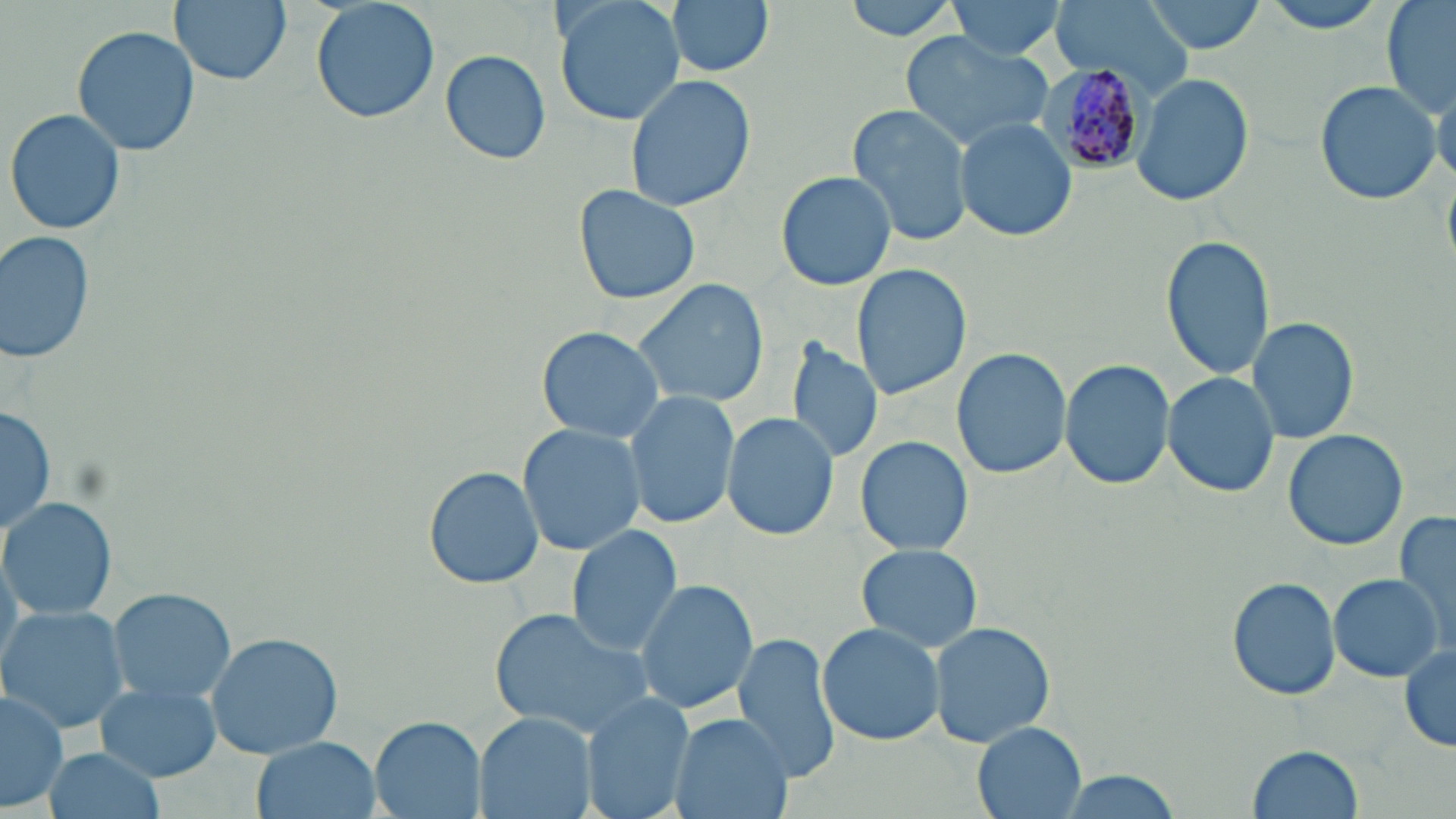

slide-level diagnosis = Plasmodium malariae
image size = 1456×819 pixels
stain = May-Grünwald-Giemsa
uninfected red blood cell locations = approximate bounding boxes as [x1, y1, x2, y2] in pixels: [170, 0, 291, 87], [309, 0, 440, 125], [552, 0, 686, 127], [665, 0, 772, 77], [839, 0, 964, 41], [945, 0, 1072, 60], [1137, 0, 1268, 53], [1257, 0, 1400, 32], [1383, 0, 1455, 116], [1054, 2, 1189, 89], [72, 26, 199, 155], [900, 32, 1053, 151], [439, 49, 553, 164], [625, 73, 757, 214], [1131, 73, 1251, 207], [1314, 81, 1442, 206], [846, 104, 975, 249], [6, 109, 125, 236], [955, 118, 1078, 242], [775, 169, 898, 292], [573, 184, 700, 306], [1, 231, 94, 366], [1160, 234, 1272, 381], [851, 265, 971, 400], [632, 277, 772, 409], [1247, 316, 1358, 445], [536, 325, 665, 444], [788, 336, 883, 466], [951, 347, 1070, 479], [1060, 357, 1175, 491], [1163, 372, 1281, 498], [624, 390, 739, 529], [1, 403, 56, 540], [721, 413, 839, 540], [517, 423, 646, 556], [1282, 428, 1409, 550], [855, 434, 975, 556], [423, 467, 543, 588], [2, 497, 117, 622], [1393, 507, 1455, 651], [568, 525, 684, 658], [855, 544, 984, 653], [1328, 574, 1445, 680], [635, 577, 759, 716], [1228, 577, 1343, 702], [109, 589, 237, 706], [1, 605, 130, 732], [488, 608, 656, 740], [930, 621, 1056, 751], [817, 623, 944, 748], [204, 631, 344, 759], [731, 635, 841, 786], [1400, 648, 1456, 751], [94, 680, 222, 783], [1, 686, 68, 812], [582, 690, 696, 819], [476, 712, 596, 819], [668, 712, 791, 819], [371, 717, 485, 819], [972, 723, 1088, 818], [251, 736, 381, 819], [1247, 743, 1367, 819], [39, 745, 165, 819], [1051, 771, 1190, 819]
modality = optical microscopy
preparation = thin blood smear
field of view = one of a larger specimen
Plasmodium malariae-infected red blood cell locations = approximate bounding boxes as [x1, y1, x2, y2] in pixels: [1039, 63, 1152, 173]
magnification = 1000x